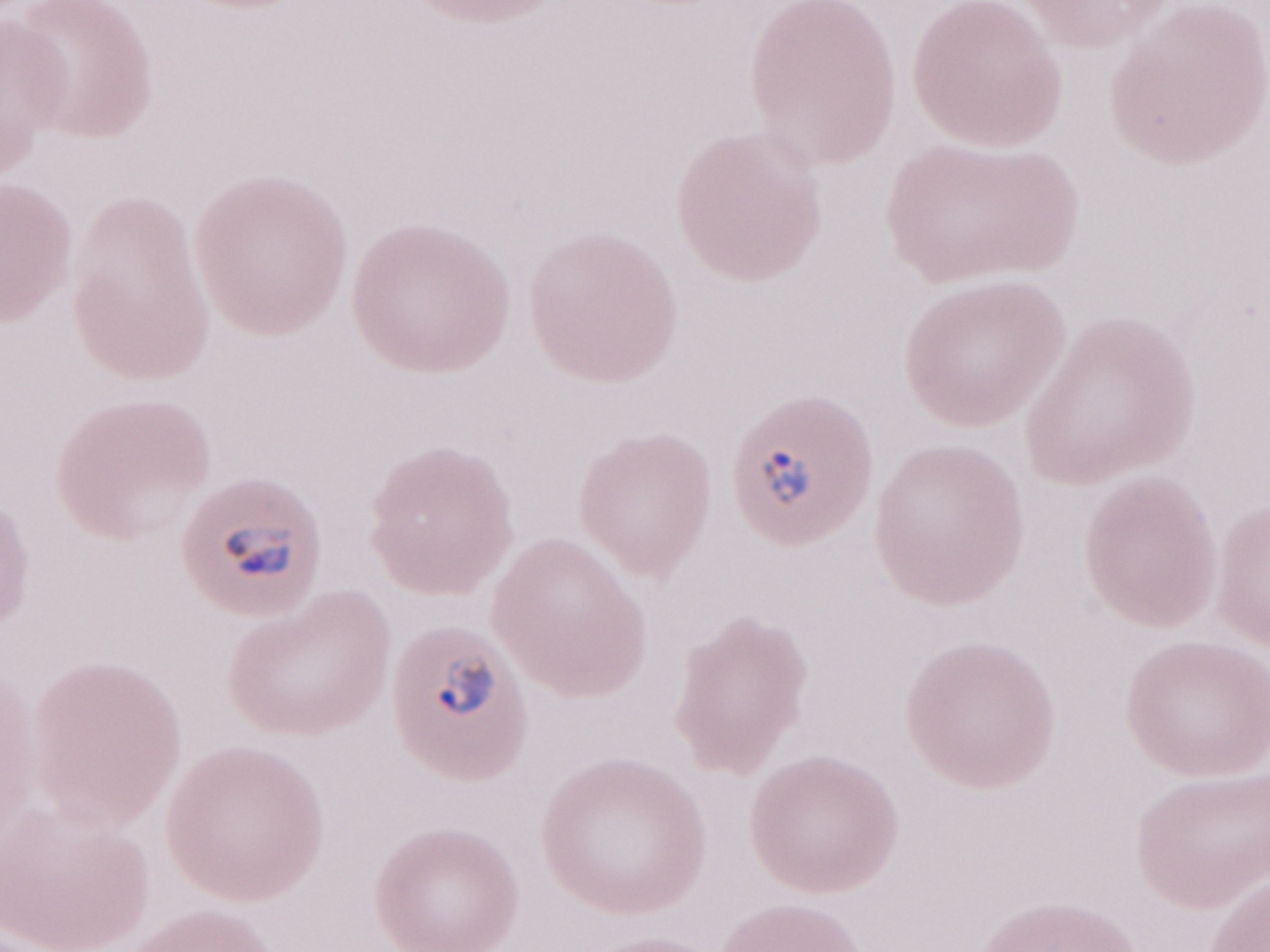

Magnification: 1,000x. May-Grünwald-Giemsa (MGG) stain. Olympus BX43 microscope and DP73 digital camera. Single field of view. Patient-level malaria diagnosis: positive. Thin peripheral-blood smear. Image is 1270×952 pixels.